Report the malaria status of this cell.
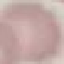
It is uninfected.

{
  "image_type": "automatically extracted cell patch, resized to 64 × 64 pixels",
  "capture": "smartphone camera at the microscope eyepiece",
  "preparation": "thin blood film",
  "stain": "Giemsa"
}